Locate every blood parasite and identify its species.
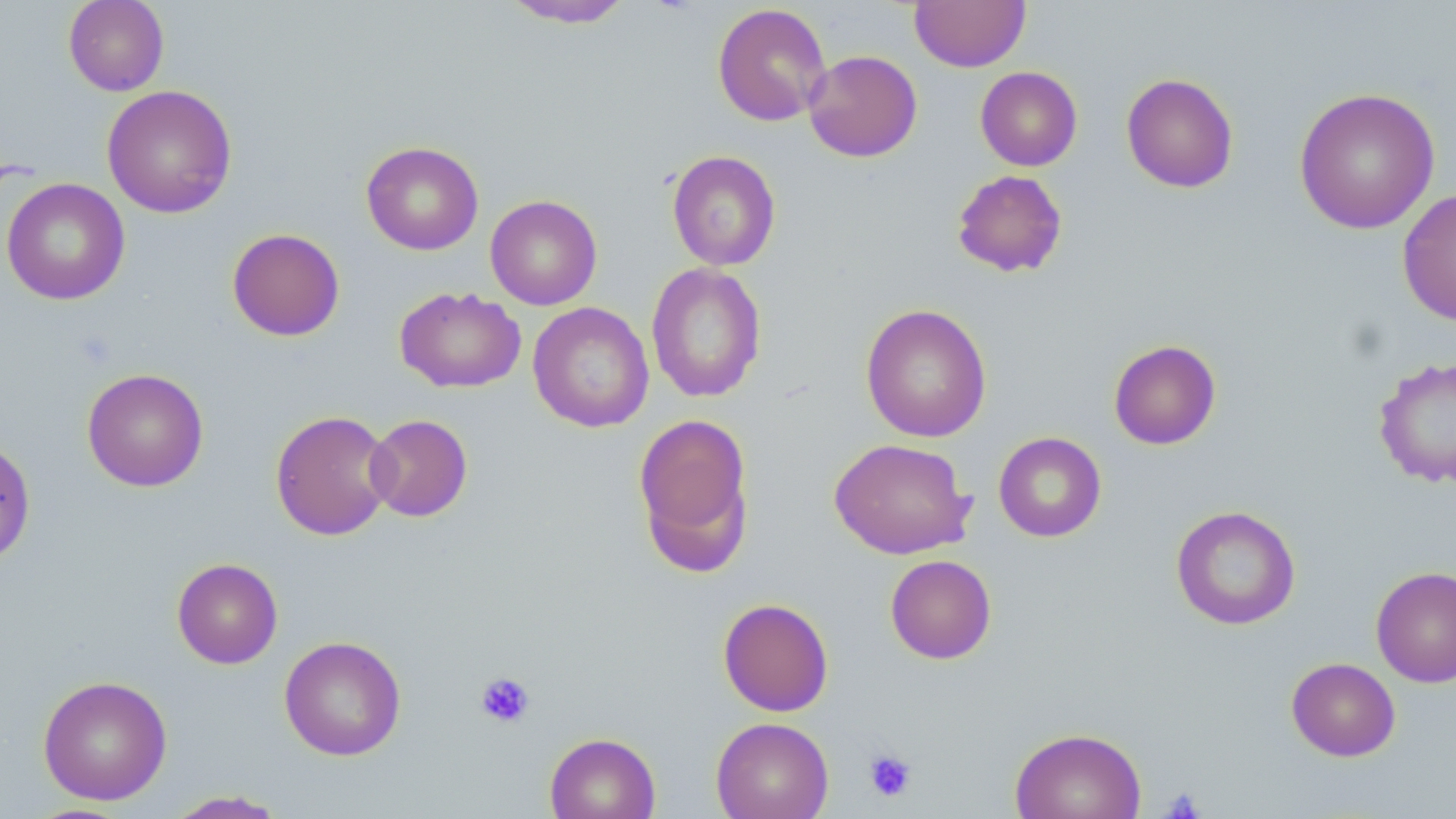

No blood parasites seen.

Approximate bounding boxes as (x1,y1)-(x2,y2) corner pairs in pixels. Platelet locations: (474,671)-(535,729), (864,748)-(916,802), (1162,787)-(1205,819). Uninfected red blood cell locations: (63,0)-(169,96), (497,0)-(638,28), (909,0)-(1031,72), (712,3)-(832,126), (803,49)-(922,162), (975,66)-(1082,171), (1120,72)-(1239,193), (102,85)-(237,218), (1293,87)-(1441,235), (361,140)-(484,255), (667,150)-(781,271), (951,169)-(1068,278), (2,178)-(130,305), (1397,188)-(1456,325), (485,195)-(602,310), (227,228)-(345,341), (646,262)-(767,403), (394,287)-(526,393), (528,301)-(654,433), (861,303)-(992,442), (1108,339)-(1221,450), (1373,356)-(1456,489), (82,368)-(209,492), (270,409)-(395,541), (633,412)-(755,573), (365,414)-(473,522), (993,431)-(1107,543), (0,436)-(36,567), (829,437)-(976,559), (1170,504)-(1301,630), (885,554)-(997,664), (172,558)-(283,669), (1371,566)-(1456,688), (717,597)-(834,717), (278,635)-(406,761), (1286,657)-(1401,761), (37,675)-(173,805), (710,717)-(834,819), (1009,727)-(1146,819), (545,731)-(661,819), (163,790)-(290,818). Slide-level diagnosis: no evidence of blood parasites. May-Grünwald-Giemsa-stained preparation. Light microscopy. Image is 1456×819 pixels. Single field of view. Captured at 1000x magnification. Thin blood smear.